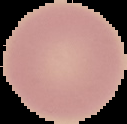
Summary:
  - Preparation: thin blood film
  - Result: no Plasmodium parasites detected
  - Image type: segmented cell region with the area outside set to black
  - Image size: 127×124 pixels